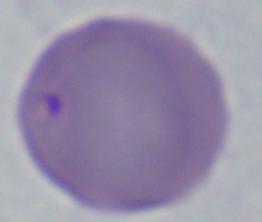
Summary:
  - Magnification: 1000x
  - Identification: Babesia
  - Modality: photomicrograph